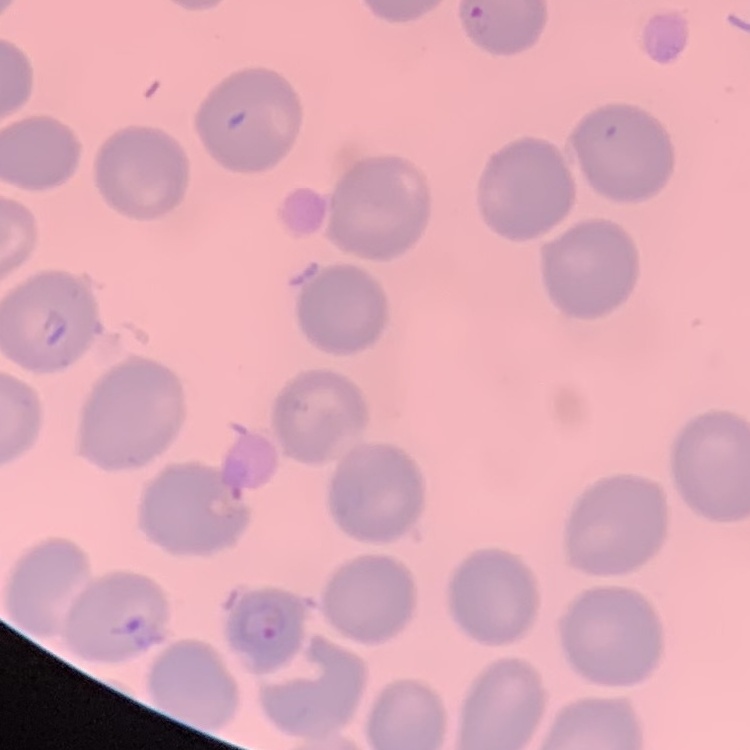
red blood cell morphology = no rouleaux formation
preparation = thin peripheral smear
stain = Field's or Giemsa
image type = one tile cut from a larger photomicrograph